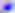
identification = Toxoplasma gondii
magnification = 400x
modality = micrograph